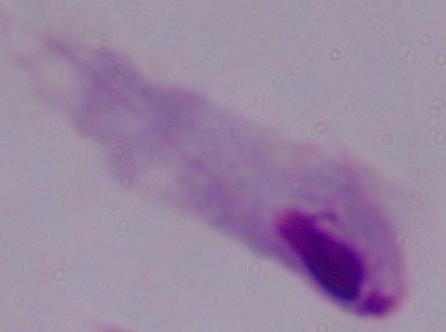

magnification = 1000x
modality = micrograph
identification = trichomonad